Give the position of every malaria parasite.
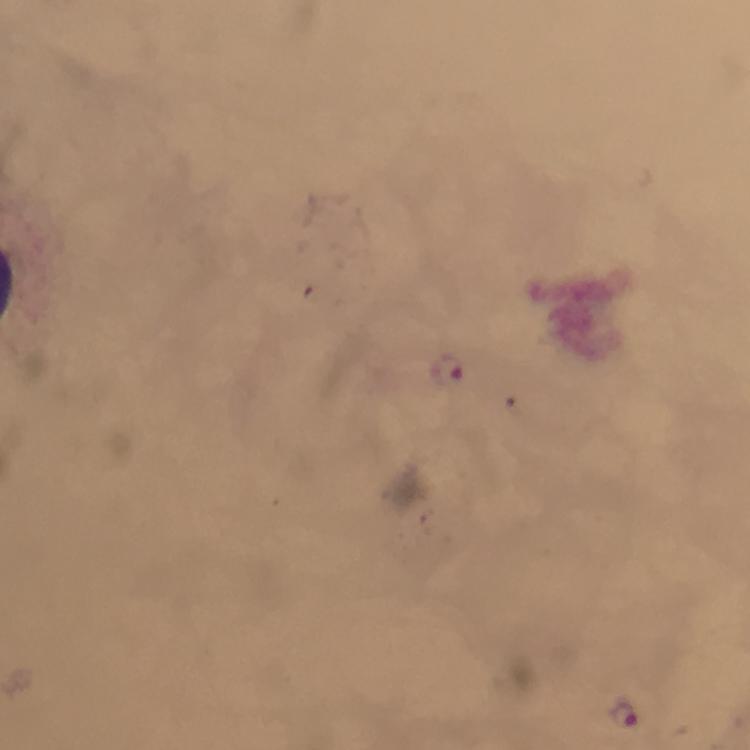
Approximate centers as (x, y) in pixels.
Malaria parasites: (448, 369), (624, 712).

image_size: 750×750 pixels
preparation: thick smear
context: from a diagnostic examination for malaria
stain: Giemsa
magnification: 100x
immersion_oil: used
capture: smartphone camera through the microscope
cropped_from: one field of view